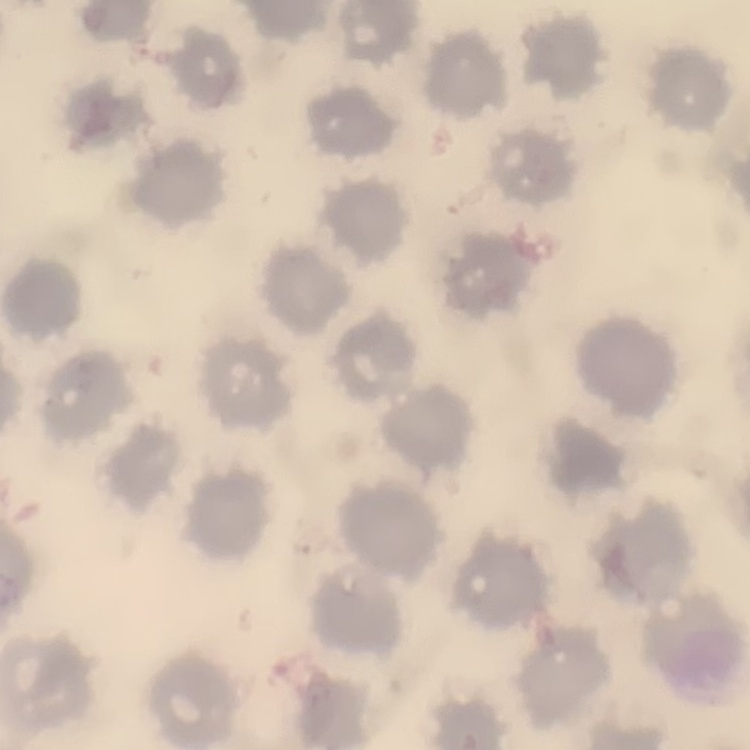
{
  "erythrocyte_morphology": "no rouleaux formation",
  "image_type": "square crop of a larger photomicrograph",
  "stain": "Field's or Giemsa",
  "preparation": "thin peripheral smear"
}